Name the parasite shown.
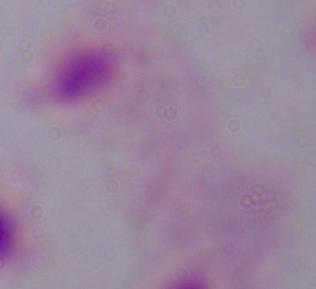

This is a trichomonad.

Summary:
  - Magnification: 1000x
  - Modality: micrograph